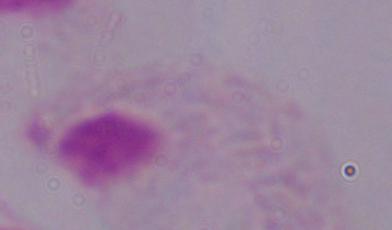

Summary:
  - Magnification: 1000x
  - Modality: photomicrograph
  - Identification: trichomonad